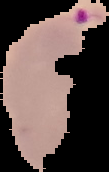

image size = 109×172 pixels
result = Plasmodium parasites detected
preparation = thin blood film
image type = segmented cell region on a black background